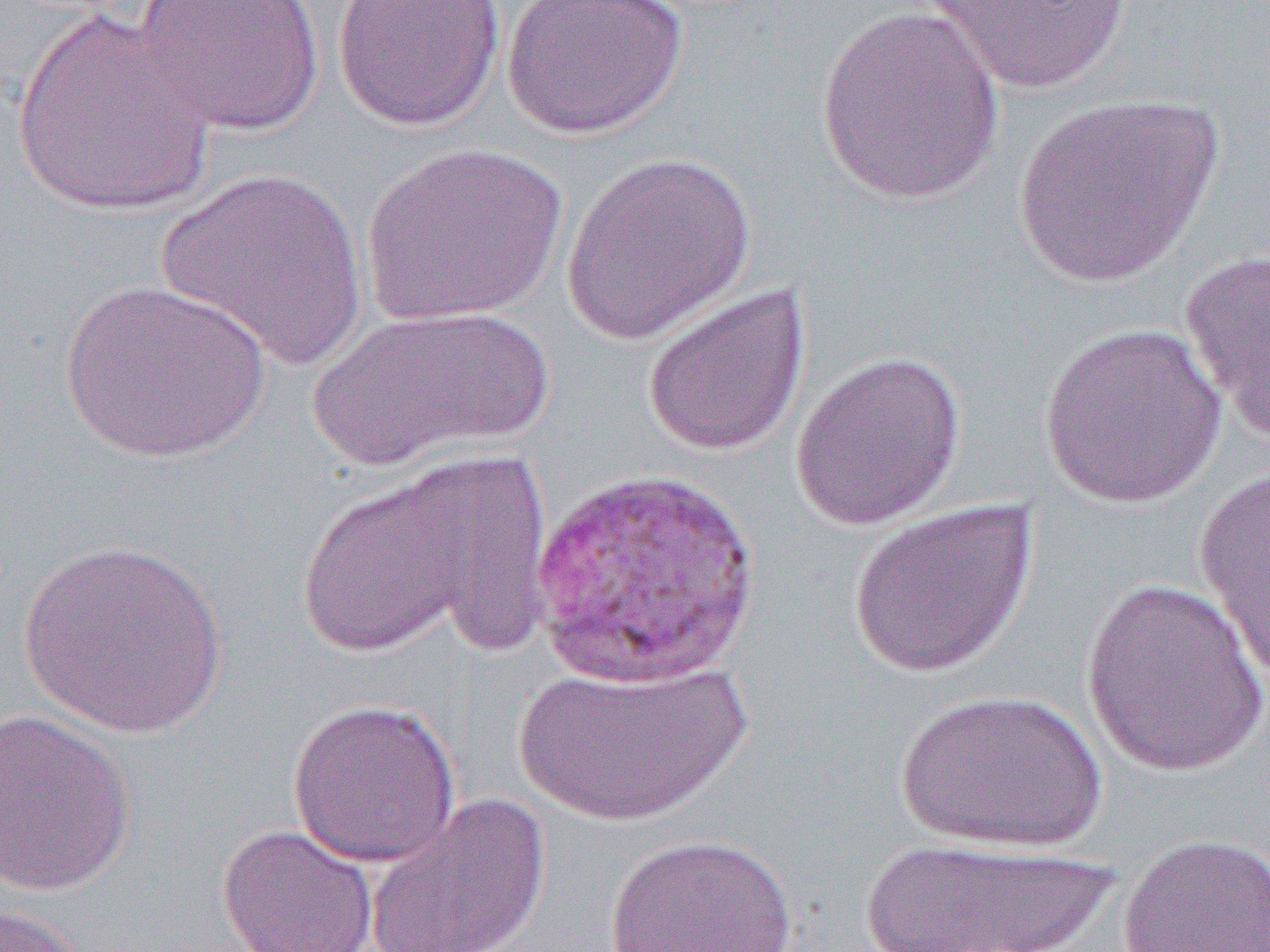
Approximate bounding boxes as [x1, y1, x2, y2] in pixels. Uninfected red blood cell locations: [131, 0, 327, 137], [332, 0, 506, 132], [501, 0, 689, 139], [924, 0, 1133, 94], [815, 6, 1005, 205], [10, 10, 217, 218], [1009, 90, 1226, 288], [361, 142, 567, 326], [560, 151, 758, 343], [156, 166, 369, 371], [1179, 248, 1270, 441], [58, 277, 273, 464], [641, 284, 812, 458], [307, 304, 554, 471], [1038, 322, 1228, 510], [790, 350, 967, 531], [379, 445, 564, 658], [291, 464, 509, 663], [1194, 465, 1270, 688], [846, 499, 1038, 679], [19, 537, 228, 740], [1079, 576, 1270, 777], [511, 659, 750, 829], [894, 688, 1107, 853], [286, 698, 461, 868], [0, 709, 137, 896], [364, 792, 551, 952], [216, 823, 379, 952], [604, 832, 801, 951], [1117, 832, 1270, 952], [857, 835, 1120, 951], [0, 900, 87, 952]. Slide-level diagnosis: Plasmodium vivax. Single field of view. Thin blood film. Optical microscopy. 1000x magnification. Image is 1270×952 pixels.